Locate every malaria parasite.
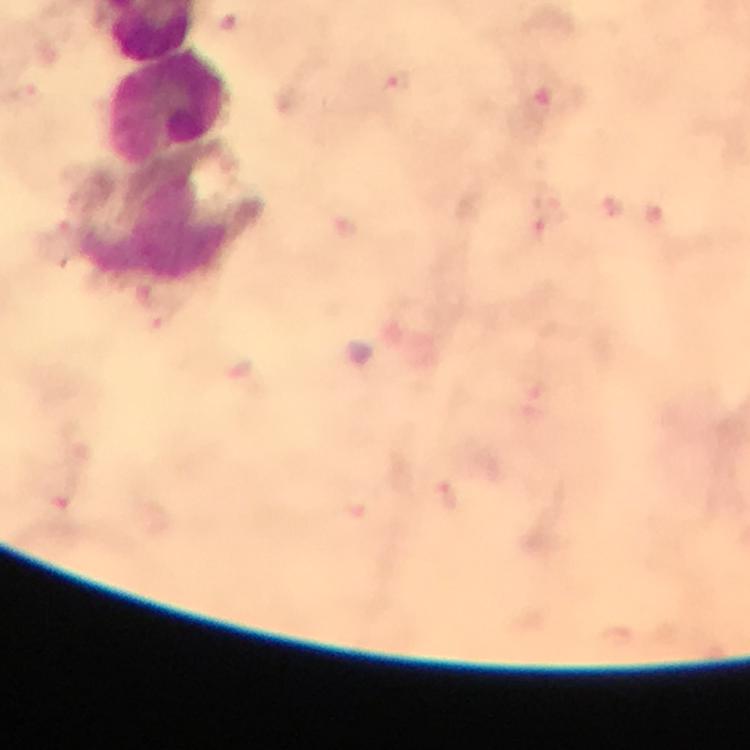

Approximate centers as [x, y] in pixels.
Malaria parasites: [396, 87], [550, 223].

Summary:
  - Leukocyte locations: [169, 108], [154, 233]
  - Stain: Giemsa
  - Immersion oil: used
  - Magnification: 100x
  - Context: from a malaria diagnostic workup
  - Preparation: thick smear
  - Capture: smartphone camera through the microscope
  - Image size: 750×750 pixels
  - Cropped from: one field of view